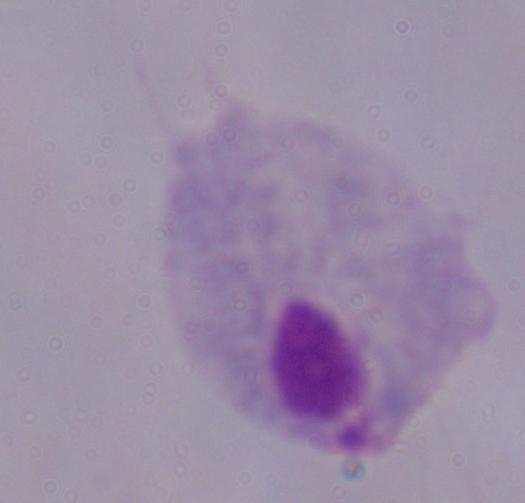
A trichomonad is seen. Photomicrograph. 1000x magnification.